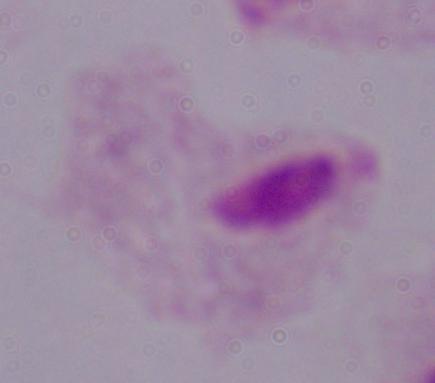
{
  "magnification": "1000x",
  "identification": "trichomonad",
  "modality": "micrograph"
}